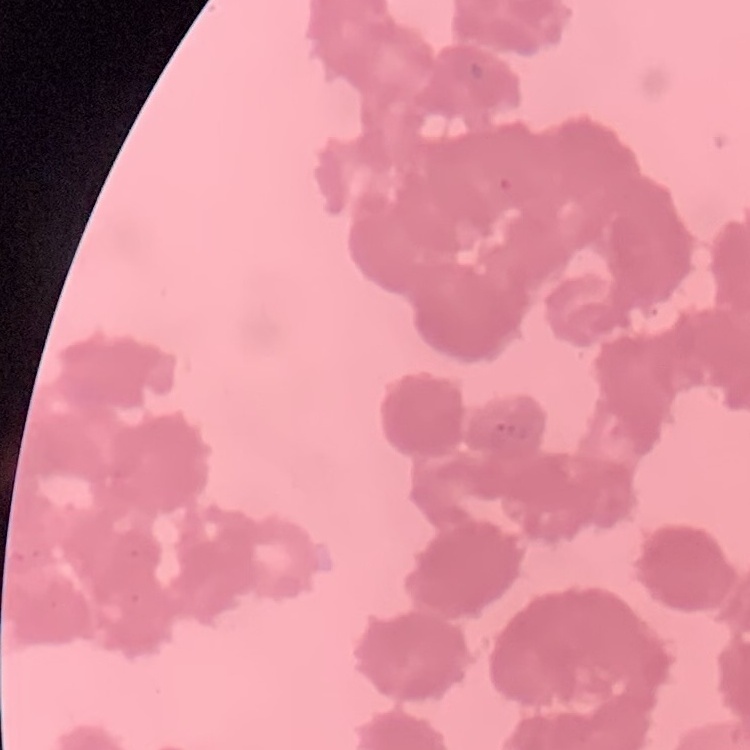
The red blood cells show rouleaux formation. Field's or Giemsa stain. Thin peripheral smear. Square crop of a larger photomicrograph.